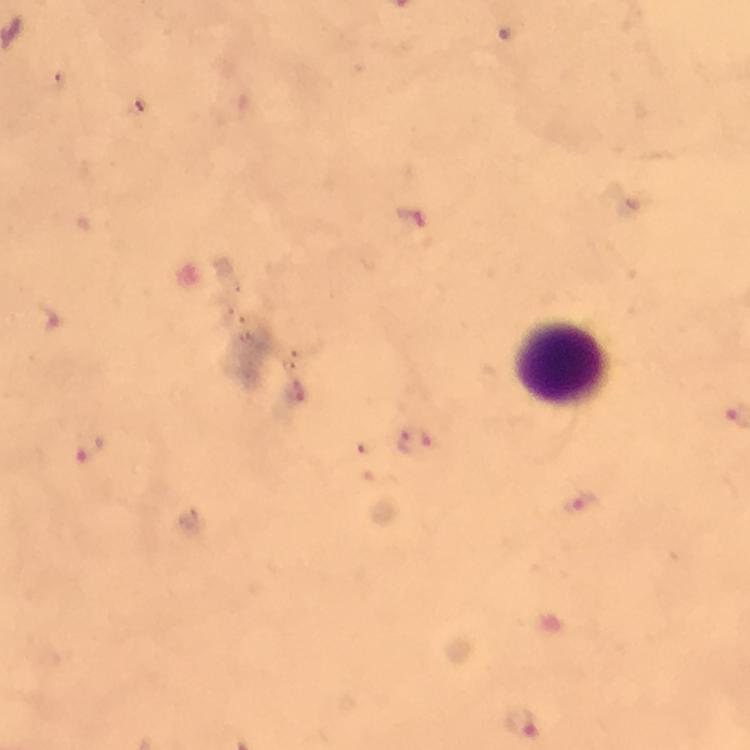
Approximate centers as [x, y] in pixels. Plasmodium parasite locations: [415, 443], [92, 450], [580, 502], [525, 722]. Leukocyte locations: [563, 360]. At 100x magnification. Smartphone photograph taken through a microscope. Image is 750×750 pixels. A crop from one field of view. Giemsa stain. Immersion oil applied. From a malaria diagnostic workup. Thick blood film.